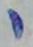
Summary:
  - Modality: photomicrograph
  - Magnification: 1000x
  - Identification: Toxoplasma gondii